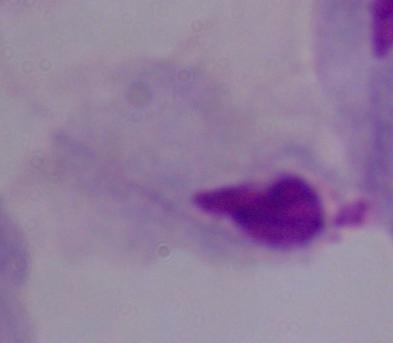
Summary:
  - Modality: micrograph
  - Magnification: 1000x
  - Identification: trichomonad